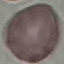

Summary:
  - Result: negative for malaria parasites
  - Capture: smartphone camera at the microscope eyepiece
  - Stain: Giemsa
  - Image type: cell patch, automatically extracted from a larger field of view and resized to 64 × 64 pixels
  - Preparation: thin blood film